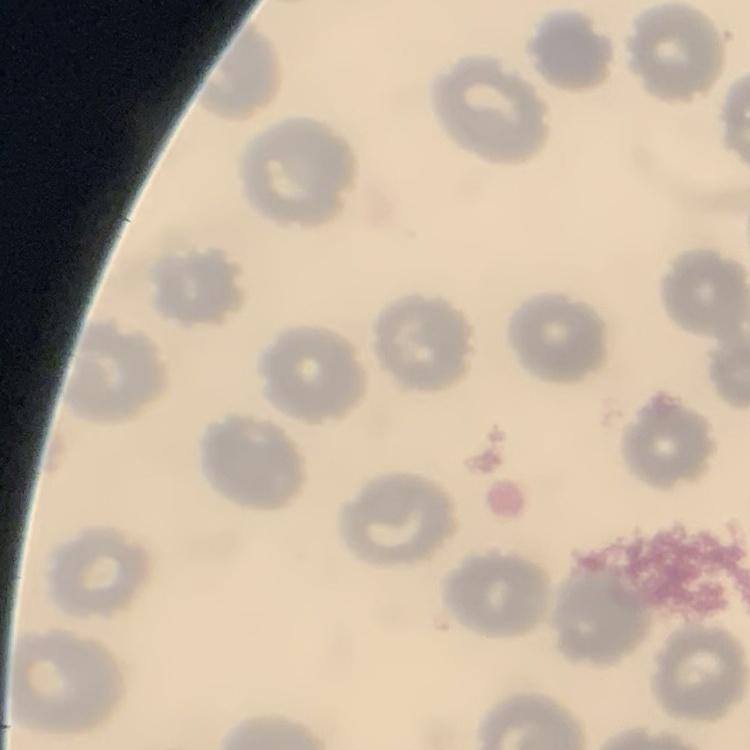
{
  "red_blood_cell_morphology": "no rouleaux formation",
  "preparation": "thin blood film",
  "stain": "Field's or Giemsa",
  "image_type": "one tile cut from a larger photomicrograph"
}